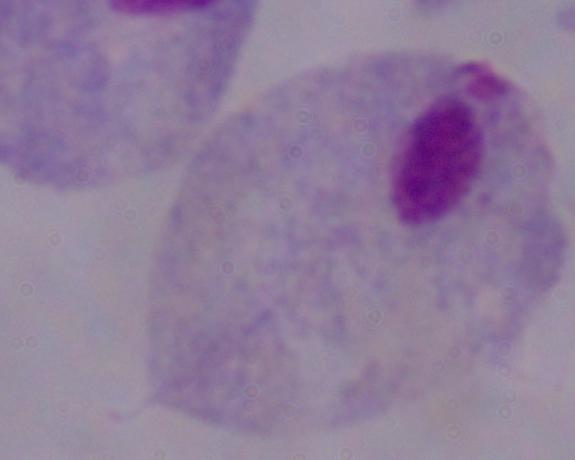

Summary:
  - Modality: photomicrograph
  - Identification: trichomonad
  - Magnification: 1000x